Identify the cell.
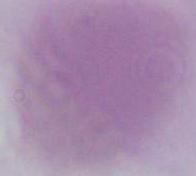

An erythrocyte.

Captured at 1000x magnification. Micrograph.